Locate every blood parasite and identify its species.
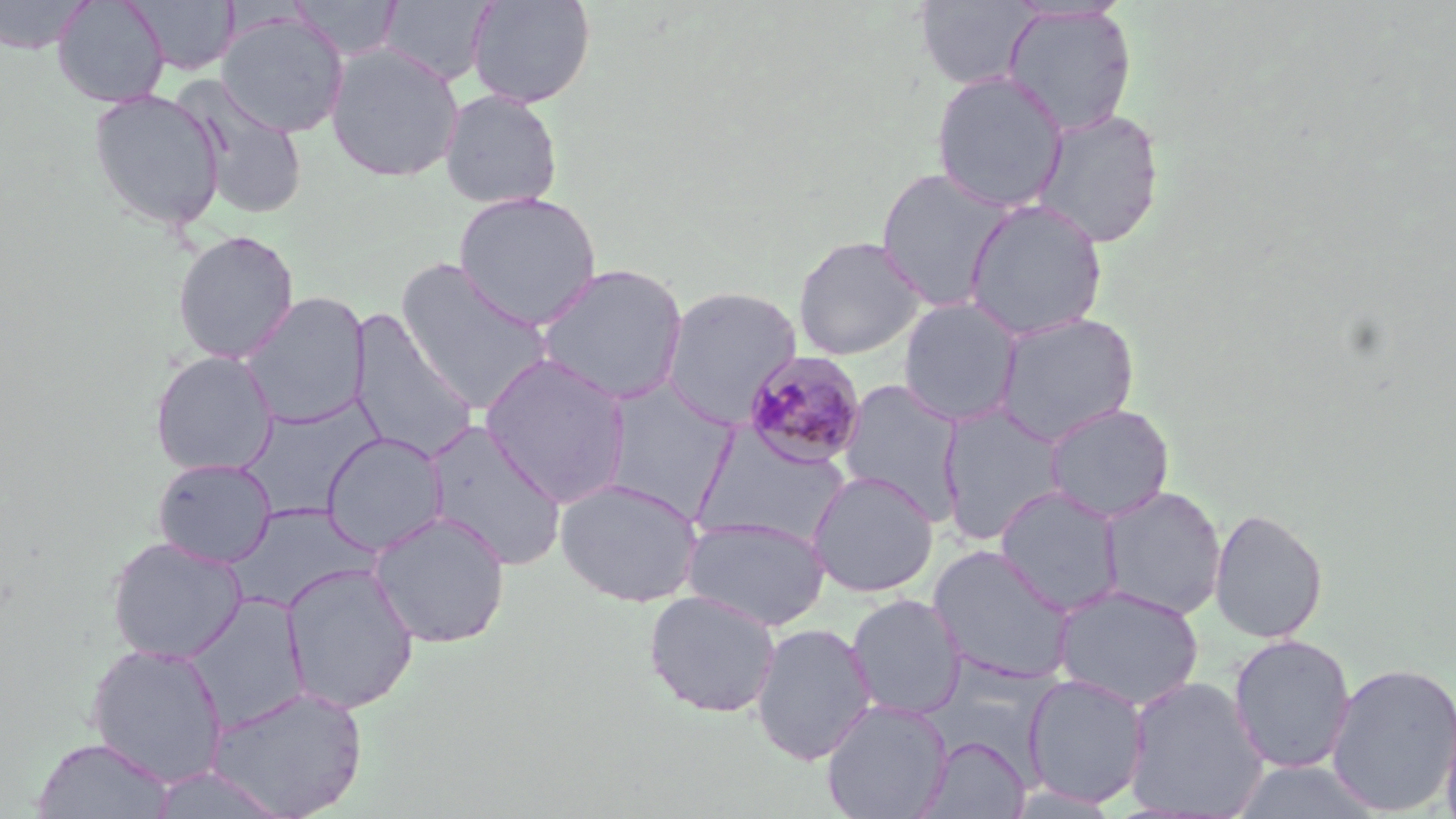

Approximate bounding boxes as [x1, y1, x2, y2] in pixels.
Plasmodium malariae-infected red blood cells: [741, 350, 868, 471].
No Plasmodium falciparum, Plasmodium ovale, Plasmodium vivax, Babesia divergens, or Trypanosoma brucei observed.

Uninfected red blood cell locations: [0, 0, 94, 55], [52, 0, 169, 108], [129, 0, 239, 75], [287, 0, 403, 60], [378, 0, 496, 86], [466, 0, 596, 108], [914, 0, 1039, 90], [1001, 4, 1137, 137], [215, 11, 350, 137], [325, 43, 464, 183], [931, 71, 1068, 212], [175, 78, 310, 220], [88, 88, 225, 232], [439, 89, 563, 210], [1031, 108, 1164, 249], [875, 167, 1018, 312], [453, 190, 602, 329], [962, 198, 1108, 342], [172, 230, 299, 363], [792, 235, 926, 360], [395, 257, 554, 415], [534, 262, 689, 405], [660, 285, 802, 428], [241, 291, 372, 429], [898, 297, 1023, 427], [346, 310, 479, 462], [993, 312, 1139, 446], [149, 350, 278, 476], [480, 352, 633, 506], [598, 378, 738, 520], [837, 378, 965, 522], [239, 398, 381, 520], [937, 402, 1068, 546], [1045, 402, 1175, 523], [424, 420, 567, 572], [321, 431, 449, 555], [152, 457, 276, 568], [806, 470, 939, 598], [555, 477, 703, 607], [995, 485, 1123, 616], [1098, 485, 1227, 620], [227, 505, 372, 613], [1209, 508, 1328, 644], [369, 510, 511, 649], [683, 515, 830, 631], [106, 536, 247, 664], [927, 544, 1074, 685], [280, 561, 419, 715], [1052, 584, 1205, 710], [643, 589, 782, 718], [184, 594, 309, 733], [846, 594, 965, 720], [750, 622, 877, 766], [1229, 634, 1356, 774], [86, 643, 228, 787], [1326, 660, 1456, 816], [1022, 673, 1150, 809], [1122, 675, 1269, 819], [206, 684, 368, 818], [1440, 697, 1456, 819], [821, 698, 952, 818], [919, 734, 1030, 818], [32, 736, 173, 818], [1227, 760, 1385, 819], [149, 766, 290, 818]. Slide-level diagnosis: Plasmodium malariae. Light microscopy. 1000x magnification. Image is 1456×819 pixels. Single field of view. Thin blood smear. May-Grünwald-Giemsa-stained preparation.